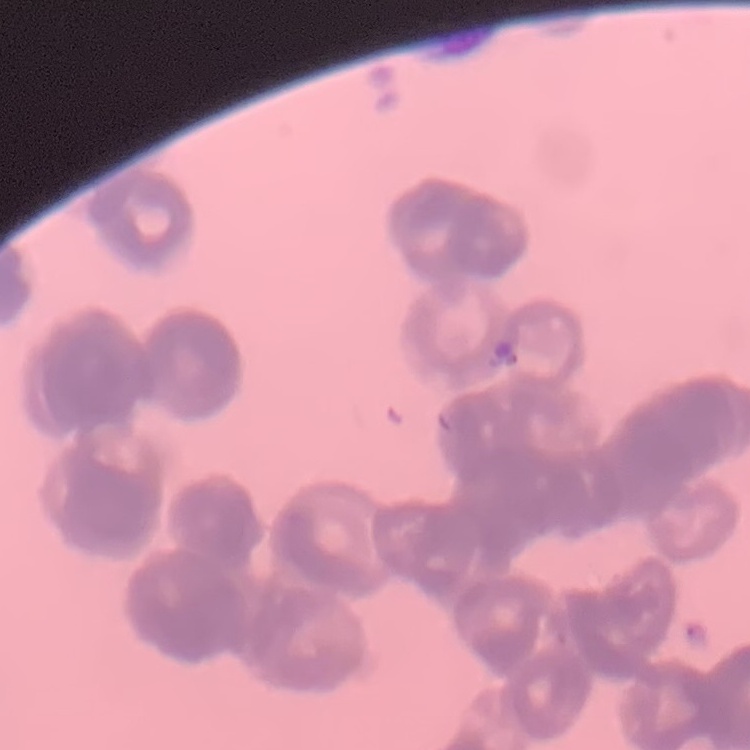

Summary:
  - Erythrocyte morphology: rouleaux formation
  - Stain: Field's or Giemsa
  - Image type: square crop of a larger photomicrograph
  - Preparation: thin blood smear